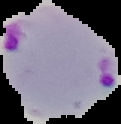
preparation = thin blood smear
result = Plasmodium parasites detected
image size = 121×124 pixels
image type = segmented cell region on a black background